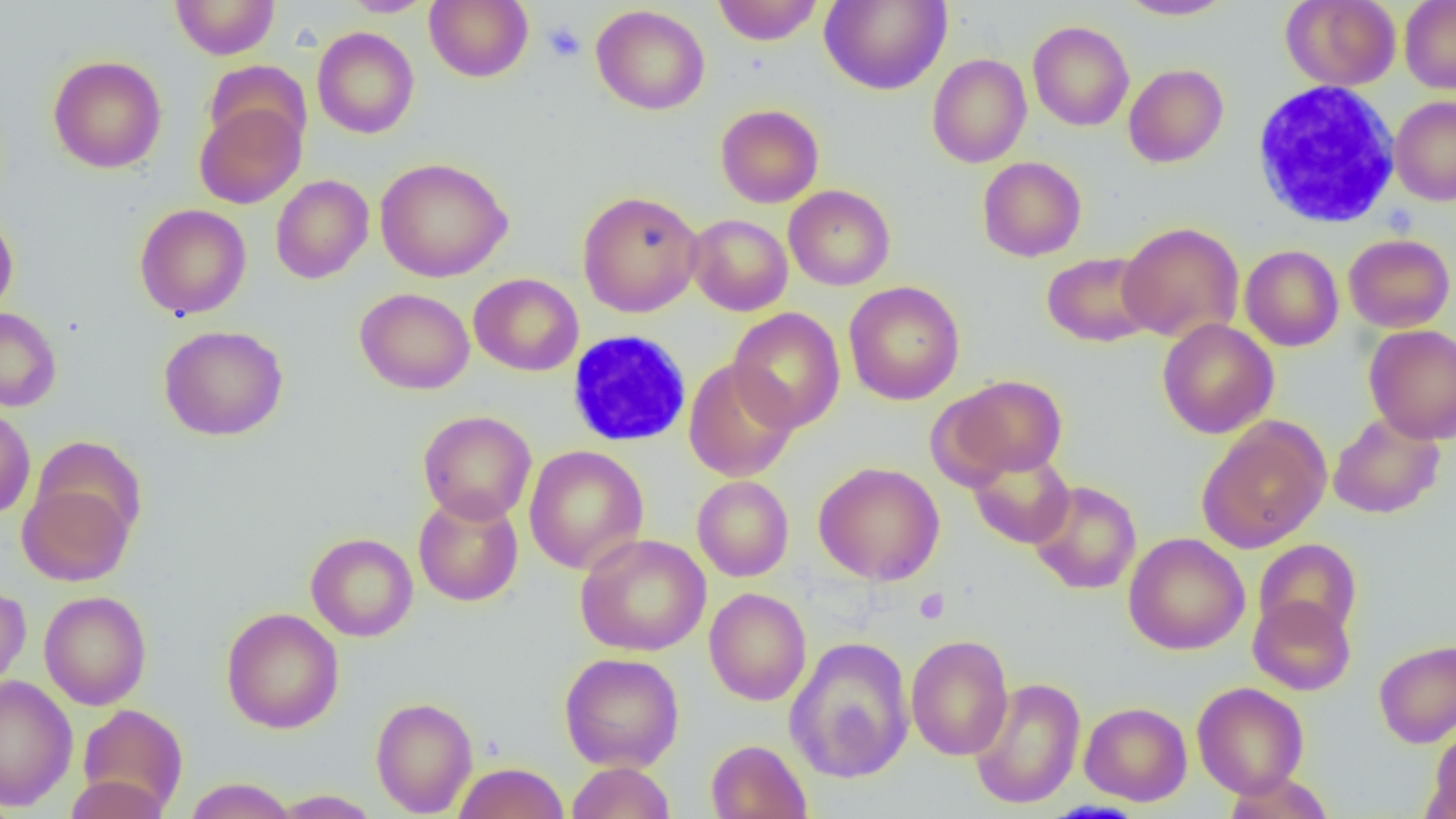 Approximate bounding boxes as [x1, y1, x2, y2] in pixels. Platelet locations: [542, 21, 586, 63], [915, 588, 950, 624]. Uninfected red blood cell locations: [170, 0, 279, 59], [340, 0, 436, 17], [424, 0, 533, 82], [713, 0, 824, 45], [819, 0, 952, 95], [1116, 0, 1234, 20], [1281, 0, 1401, 90], [1399, 0, 1456, 94], [591, 4, 710, 115], [1028, 20, 1134, 131], [312, 26, 419, 138], [927, 53, 1031, 168], [48, 55, 166, 173], [203, 60, 313, 153], [1123, 63, 1229, 167], [1390, 96, 1456, 206], [194, 101, 306, 209], [715, 104, 824, 208], [977, 156, 1086, 262], [375, 157, 513, 282], [271, 175, 373, 284], [784, 185, 895, 291], [577, 190, 704, 317], [135, 204, 252, 319], [0, 212, 18, 318], [686, 214, 793, 316], [1118, 221, 1244, 343], [1343, 234, 1455, 332], [1239, 242, 1453, 341], [1240, 245, 1343, 351], [1042, 251, 1157, 347], [469, 272, 583, 376], [843, 281, 964, 405], [354, 287, 475, 395], [728, 301, 963, 422], [0, 307, 62, 411], [728, 307, 845, 434], [1157, 318, 1279, 439], [158, 324, 288, 441], [1364, 324, 1456, 444], [683, 359, 798, 482], [946, 375, 1069, 480], [0, 407, 35, 519], [418, 410, 536, 524], [1328, 412, 1446, 519], [1197, 418, 1331, 553], [523, 445, 649, 574], [968, 447, 1075, 549], [813, 461, 945, 585], [692, 475, 794, 582], [1028, 480, 1142, 594], [18, 481, 136, 586], [413, 493, 523, 606], [1123, 532, 1250, 655], [305, 533, 418, 641], [575, 533, 712, 656], [1254, 539, 1362, 640], [0, 585, 31, 694], [704, 587, 811, 705], [39, 590, 151, 710], [1248, 595, 1356, 696], [221, 607, 344, 733], [906, 634, 1014, 760], [785, 636, 915, 784], [1373, 639, 1456, 748], [559, 652, 684, 772], [0, 675, 78, 811], [969, 677, 1086, 809], [1191, 681, 1309, 797], [371, 696, 477, 816], [1079, 701, 1192, 806], [77, 704, 188, 815], [1427, 727, 1456, 819], [706, 739, 812, 819], [566, 761, 675, 818], [453, 762, 570, 819], [1222, 772, 1333, 818], [65, 775, 167, 819], [184, 777, 296, 819], [270, 790, 383, 818]. White blood cell locations: [1251, 80, 1402, 228], [568, 327, 693, 446]. Slide-level diagnosis: no evidence of blood parasites. Thin blood smear. One field of a larger specimen. Image is 1456×819 pixels. Optical microscopy. Captured at 1000x magnification.